Outline each uninfected red blood cell.
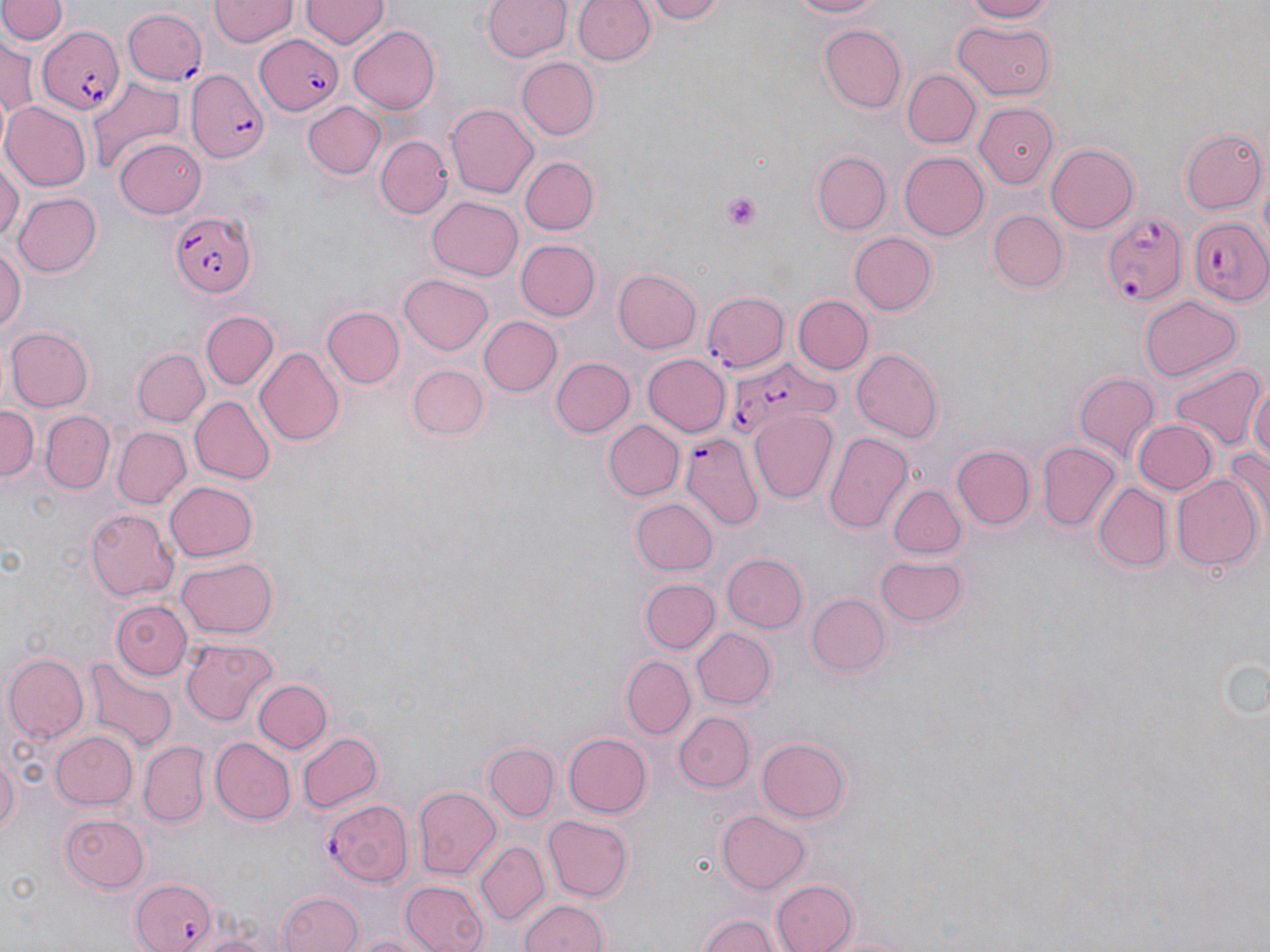
Approximate bounding boxes as (x1,y1)-(x2,y2) corner pairs in pixels.
Uninfected red blood cells: (209,0)-(296,47), (299,0)-(387,50), (574,0)-(655,66), (642,0)-(730,24), (780,0)-(890,19), (957,0)-(1061,23), (0,1)-(64,48), (482,1)-(572,63), (953,17)-(1057,101), (819,24)-(907,113), (347,25)-(442,114), (1,38)-(37,125), (518,58)-(600,140), (903,68)-(981,146), (86,77)-(184,172), (2,99)-(92,191), (973,99)-(1061,190), (301,100)-(387,181), (448,103)-(539,199), (1181,128)-(1266,214), (373,135)-(451,220), (114,136)-(207,218), (1045,143)-(1140,233), (812,151)-(891,234), (898,151)-(989,241), (521,157)-(596,235), (0,159)-(21,248), (11,191)-(102,279), (427,197)-(522,280), (988,210)-(1067,292), (849,232)-(936,315), (516,239)-(600,321), (0,243)-(25,334), (513,248)-(687,334), (613,267)-(702,354), (399,273)-(494,356), (1138,294)-(1243,381), (792,295)-(873,375), (322,305)-(405,388), (199,309)-(280,390), (476,315)-(563,399), (5,326)-(92,412), (253,346)-(343,446), (850,347)-(943,442), (133,348)-(208,425), (642,354)-(732,438), (551,356)-(636,438), (1170,362)-(1264,451), (408,364)-(487,441), (1074,374)-(1161,466), (1248,377)-(1270,472), (188,396)-(275,485), (0,405)-(39,486), (746,408)-(838,502), (42,410)-(116,493), (602,419)-(684,501), (1132,419)-(1219,495), (112,426)-(191,510), (824,432)-(914,536), (1036,442)-(1121,532), (949,444)-(1036,531), (1224,445)-(1270,532), (1170,474)-(1262,572), (163,480)-(258,563), (889,483)-(966,558), (1093,484)-(1173,572), (629,497)-(718,576), (86,506)-(179,598), (722,552)-(807,632), (175,554)-(277,640), (875,555)-(967,627), (638,578)-(719,655), (805,593)-(890,677), (111,597)-(192,680), (692,628)-(776,710), (181,637)-(278,726), (5,653)-(88,743), (621,653)-(696,738), (82,656)-(176,754), (252,678)-(333,754), (673,710)-(753,792), (48,730)-(138,810), (296,730)-(383,814), (563,732)-(652,818), (757,736)-(851,823), (210,738)-(296,825), (139,742)-(210,828), (484,743)-(558,822), (0,750)-(19,842), (412,786)-(503,877), (58,808)-(151,892), (715,809)-(810,894), (542,814)-(635,902), (475,842)-(549,926), (399,880)-(488,952), (772,880)-(859,952), (280,891)-(363,952), (517,898)-(609,952), (697,910)-(784,952), (192,931)-(278,952), (347,931)-(436,952).

Platelet locations: (718,192)-(764,233). Plasmodium falciparum-infected red blood cell locations: (120,8)-(209,85), (37,25)-(126,115), (252,34)-(346,115), (185,70)-(269,163), (170,210)-(256,299), (1103,211)-(1186,307), (1187,217)-(1270,306), (702,293)-(791,373), (728,355)-(835,435), (683,436)-(763,533), (325,800)-(416,888), (129,877)-(219,952). Slide-level diagnosis: Plasmodium falciparum. Optical microscopy. Thin blood smear. May-Grünwald-Giemsa-stained preparation. Image is 1270×952 pixels. Captured at 1000x magnification. Single field of view.